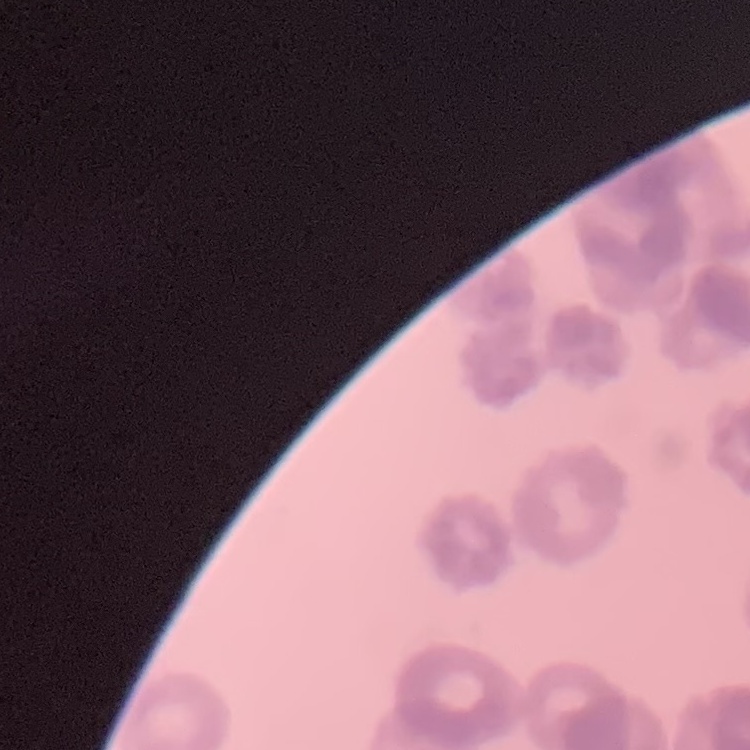
Summary:
  - Erythrocyte morphology: rouleaux formation
  - Preparation: thin blood film
  - Stain: Field's or Giemsa
  - Image type: square crop of a larger photomicrograph